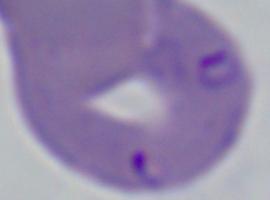 Photomicrograph. A Babesia parasite is shown. Captured at 1000x magnification.